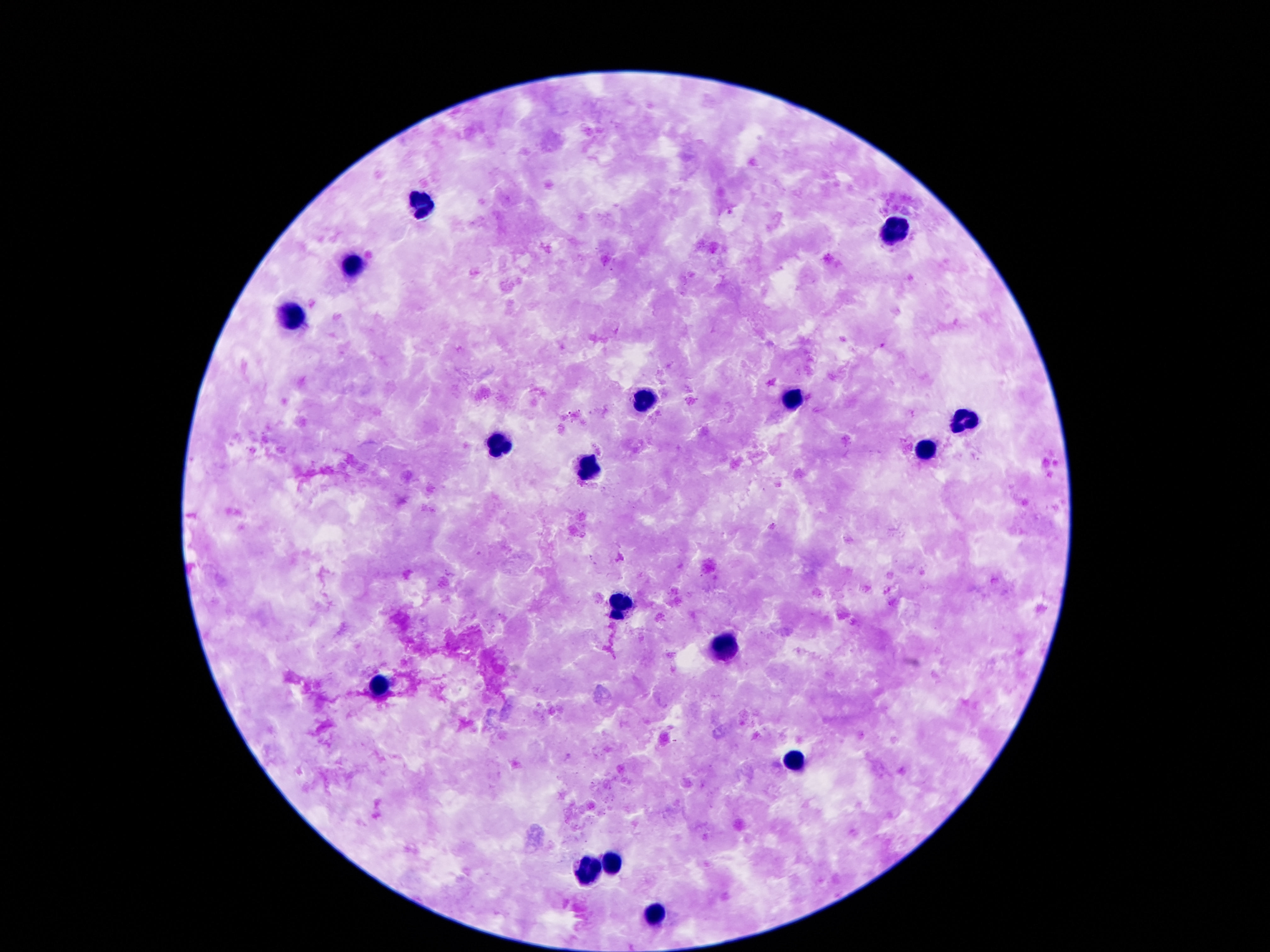
Approximate centers as (x, y) in pixels. Leukocyte locations: (421, 202), (897, 233), (354, 265), (294, 315), (794, 400), (645, 401), (966, 421), (497, 446), (923, 452), (585, 474), (624, 601), (725, 651), (380, 687), (792, 761), (612, 865), (585, 872), (655, 918). Image is 1270×952 pixels. Patient malaria status: uninfected. Photographed through the microscope eyepiece with a smartphone camera. Thick peripheral-blood smear. Single field of view. 100x magnification. Giemsa-stained preparation.